Comment on the morphology of the red blood cells.
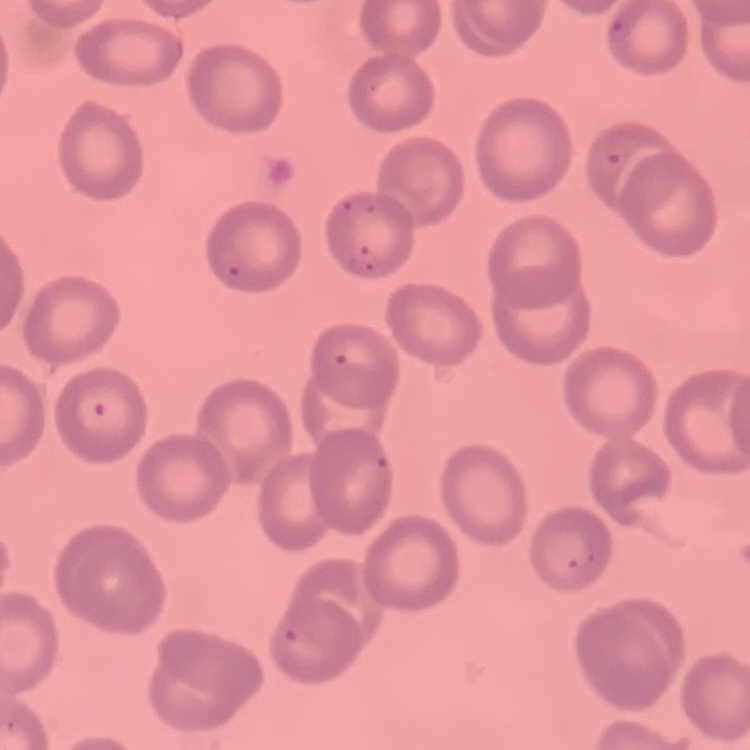
They show no rouleaux formation.

One tile cut from a larger photomicrograph. Stained with either Field's or Giemsa. Thin blood film.